Classify this cell by malaria status.
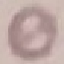
It is uninfected.

Summary:
  - Image type: cell patch, automatically extracted from a larger field of view and resized to 64 × 64 pixels
  - Preparation: thin blood smear
  - Capture: smartphone camera at the microscope eyepiece
  - Stain: Giemsa